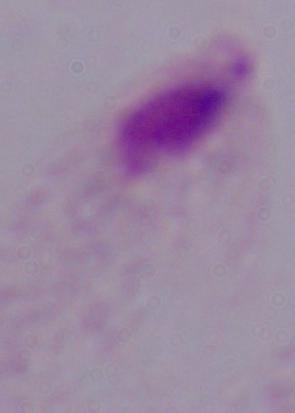

Summary:
  - Magnification: 1000x
  - Modality: micrograph
  - Identification: trichomonad